State which cell type is depicted.
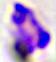
A leukocyte.

Summary:
  - Magnification: 400x
  - Modality: micrograph